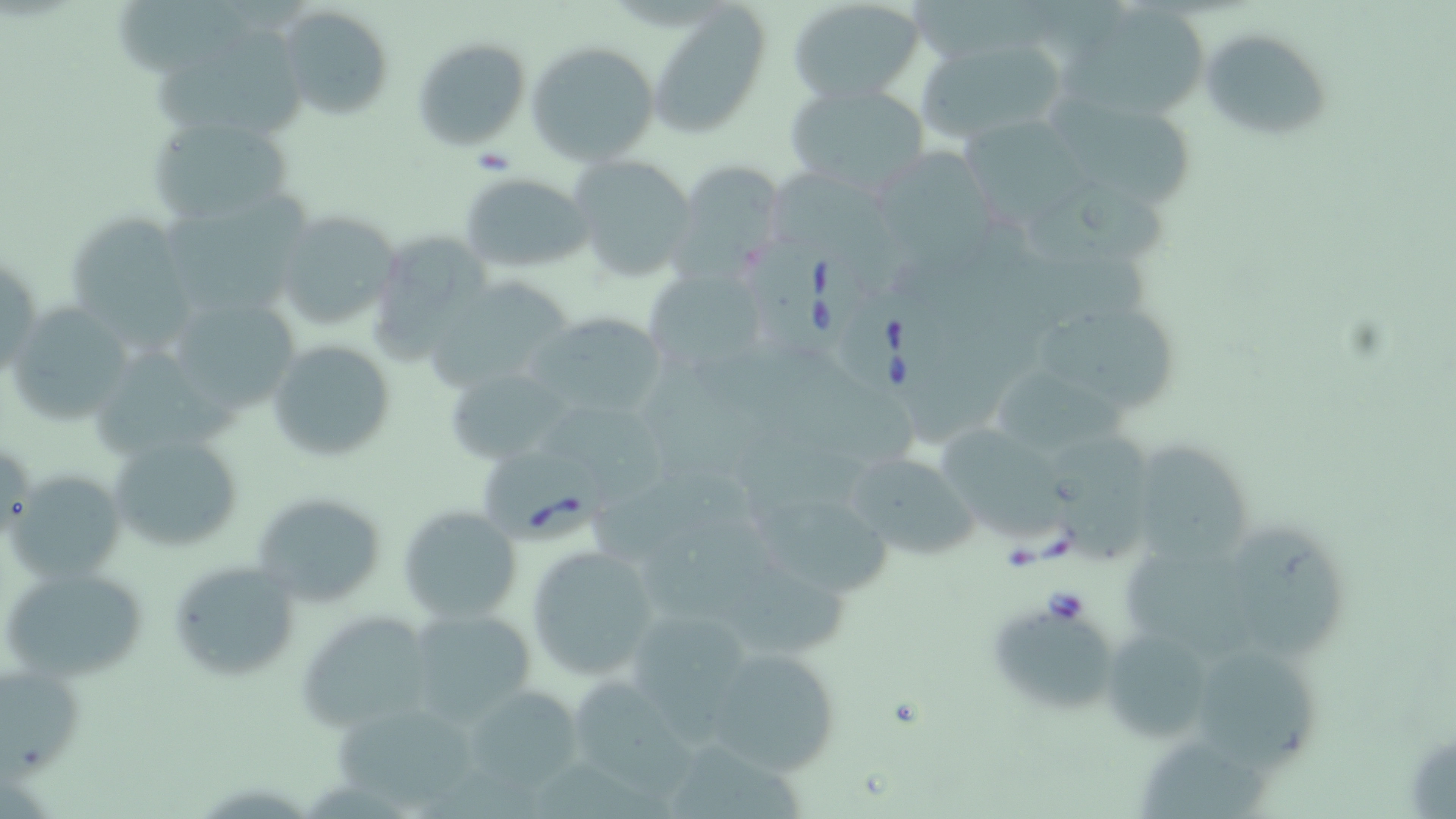

Approximate bounding boxes as (x1,y1)-(x2,y2) corner pairs in pixels. Uninfected red blood cell locations: (116,0)-(254,75), (789,1)-(926,104), (648,2)-(771,138), (1066,3)-(1215,119), (276,5)-(394,119), (1198,26)-(1333,144), (412,35)-(531,150), (915,37)-(1069,146), (526,39)-(662,166), (158,40)-(306,135), (783,80)-(930,193), (1049,95)-(1194,204), (146,111)-(296,225), (963,112)-(1102,228), (875,140)-(1009,273), (568,155)-(699,282), (672,158)-(788,280), (765,169)-(899,268), (459,172)-(592,273), (1025,173)-(1174,271), (155,187)-(318,316), (273,209)-(403,334), (64,215)-(200,347), (364,228)-(496,366), (1,250)-(44,381), (642,268)-(765,373), (425,276)-(577,396), (159,290)-(306,422), (6,302)-(136,428), (1039,308)-(1175,412), (523,312)-(673,420), (267,338)-(398,462), (645,356)-(751,477), (446,365)-(572,465), (991,365)-(1128,460), (547,412)-(666,508), (944,426)-(1070,542), (1048,431)-(1152,564), (107,432)-(244,556), (1134,438)-(1258,570), (841,450)-(983,562), (7,471)-(124,581), (589,475)-(757,568), (250,492)-(385,607), (758,499)-(890,593), (398,506)-(522,625), (644,522)-(786,633), (1239,527)-(1344,660), (526,545)-(661,679), (1122,549)-(1274,661), (170,560)-(300,681), (1,565)-(152,682), (727,566)-(850,657), (408,608)-(537,722), (997,613)-(1112,710), (300,614)-(436,729), (1106,633)-(1213,737), (702,646)-(844,777), (1199,648)-(1317,774), (0,661)-(84,772), (576,674)-(700,805), (459,683)-(586,795), (332,700)-(481,808), (1142,734)-(1269,819), (672,743)-(808,819). Babesia divergens-infected red blood cell locations: (745,230)-(863,354), (828,285)-(949,407), (484,447)-(610,544). Slide-level diagnosis: Babesia divergens. One field of a larger specimen. Thin blood smear. Captured at 1000x magnification. Image is 1456×819 pixels. May-Grünwald-Giemsa stain. Light microscopy.